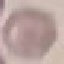 Malaria status: uninfected. Giemsa stain. Thin blood film. Cell patch, automatically extracted from a larger field of view and resized to 64 × 64 pixels. Photographed with a smartphone camera at the microscope eyepiece.